Classify this cell by malaria status.
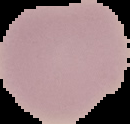
It is uninfected.

Image is 130×124 pixels. From a thin blood film. The area outside the segmented cell region is set to black.